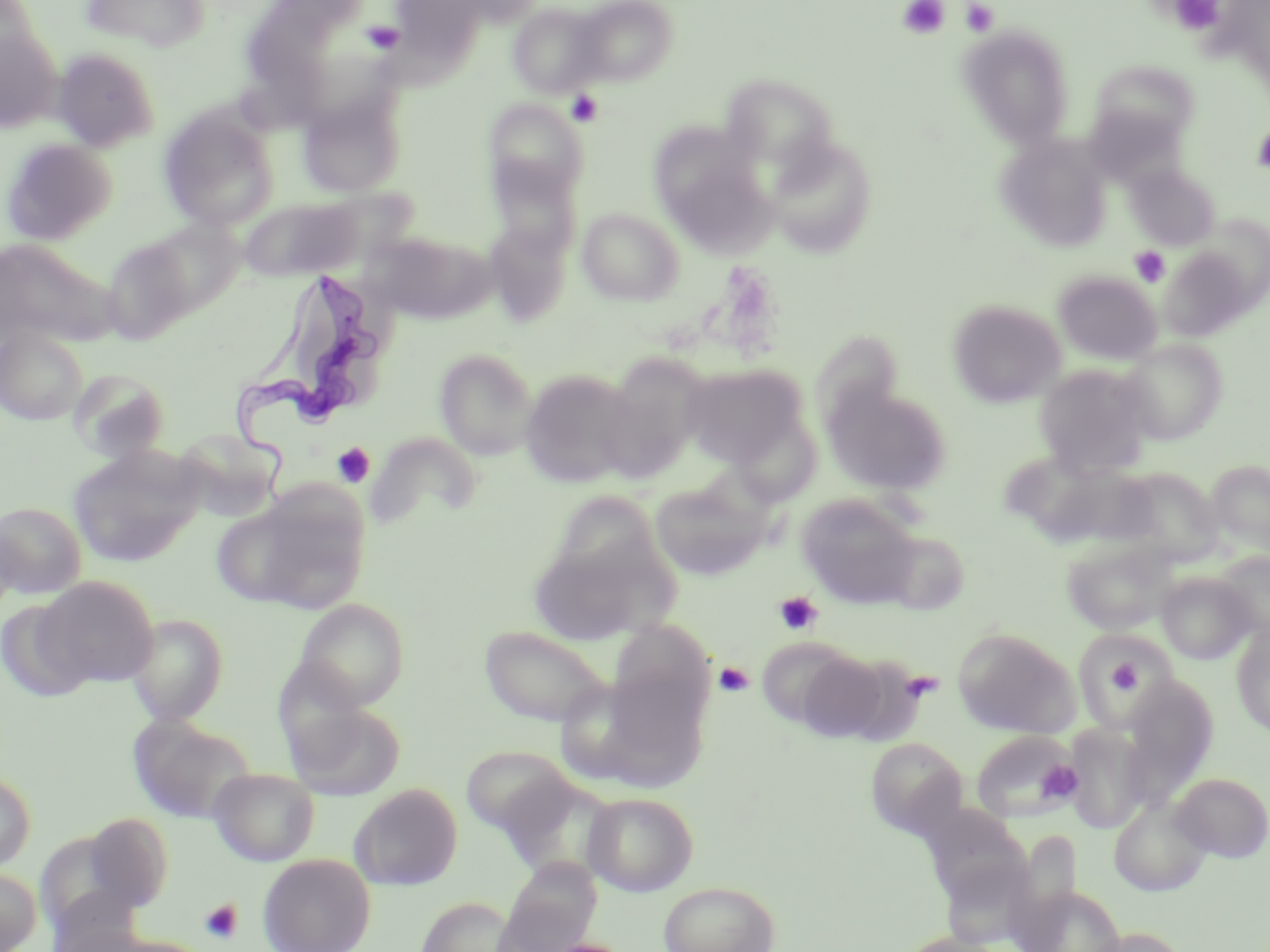

Approximate bounding boxes as (x1, y1, x2, y2) in pixels. Trypanosoma brucei locations: (234, 272, 381, 493). Uninfected red blood cell locations: (78, 0, 211, 52), (386, 0, 496, 58), (570, 0, 677, 86), (0, 1, 38, 69), (245, 1, 342, 89), (507, 3, 608, 99), (959, 26, 1074, 147), (0, 28, 63, 133), (52, 46, 162, 150), (1089, 58, 1201, 151), (720, 74, 841, 177), (298, 93, 405, 198), (485, 99, 587, 202), (159, 107, 280, 231), (653, 126, 774, 250), (764, 131, 878, 258), (996, 135, 1112, 252), (1, 138, 117, 245), (490, 155, 579, 259), (1125, 163, 1220, 251), (240, 196, 363, 281), (576, 206, 685, 306), (131, 217, 245, 324), (485, 221, 572, 326), (366, 230, 491, 324), (99, 233, 200, 344), (0, 239, 116, 349), (1159, 245, 1258, 341), (1053, 270, 1162, 365), (948, 299, 1065, 408), (0, 326, 87, 424), (810, 335, 905, 416), (1117, 339, 1228, 443), (434, 348, 538, 460), (596, 356, 710, 482), (1034, 363, 1153, 477), (681, 364, 806, 467), (67, 367, 171, 463), (519, 368, 639, 488), (824, 383, 951, 495), (174, 426, 285, 515), (366, 431, 482, 528), (67, 445, 204, 567), (1012, 454, 1156, 549), (1205, 459, 1270, 558), (1119, 465, 1223, 573), (649, 478, 769, 580), (214, 488, 369, 614), (796, 493, 921, 608), (546, 494, 665, 587), (1, 501, 87, 597), (0, 513, 20, 620), (875, 530, 969, 614), (528, 533, 669, 646), (1061, 536, 1178, 635), (1214, 551, 1270, 641), (1157, 571, 1255, 664), (38, 577, 159, 687), (293, 598, 410, 711), (1, 600, 96, 703), (126, 612, 230, 725), (479, 624, 614, 728), (1231, 625, 1270, 737), (953, 627, 1079, 738), (1072, 630, 1177, 729), (757, 637, 864, 730), (794, 651, 893, 743), (561, 659, 709, 794), (1119, 676, 1220, 796), (286, 700, 405, 800), (127, 716, 258, 824), (1064, 725, 1152, 833), (971, 730, 1081, 824), (864, 737, 969, 839), (460, 745, 575, 836), (209, 767, 321, 866), (0, 768, 36, 873), (1170, 772, 1270, 863), (349, 783, 463, 891), (582, 792, 698, 896), (1109, 796, 1213, 897), (919, 802, 1030, 906), (83, 813, 173, 912), (258, 853, 376, 952), (498, 860, 601, 952), (0, 867, 42, 952), (658, 881, 781, 952), (1022, 885, 1127, 952), (417, 896, 518, 951), (1089, 926, 1187, 952). Platelet locations: (898, 0, 950, 39), (960, 0, 999, 37), (1168, 0, 1226, 36), (363, 21, 404, 54), (566, 90, 603, 127), (1251, 125, 1270, 173), (1129, 246, 1171, 287), (332, 442, 376, 488), (773, 591, 823, 636), (1082, 640, 1166, 717), (1104, 654, 1144, 701), (714, 662, 754, 697), (1038, 761, 1082, 801), (200, 899, 243, 943). Slide-level diagnosis: Trypanosoma brucei. Image is 1270×952 pixels. Thin blood smear. One field of a larger specimen. 1000x magnification. May-Grünwald-Giemsa stain. Optical microscopy.